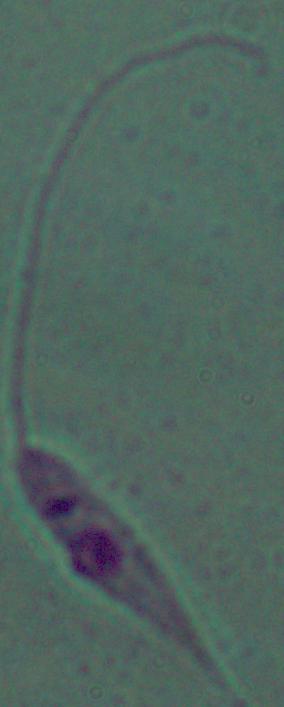
modality: photomicrograph
magnification: 1000x
identification: Leishmania